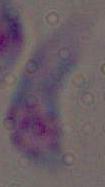
Micrograph. Toxoplasma gondii is seen. Captured at 1000x magnification.